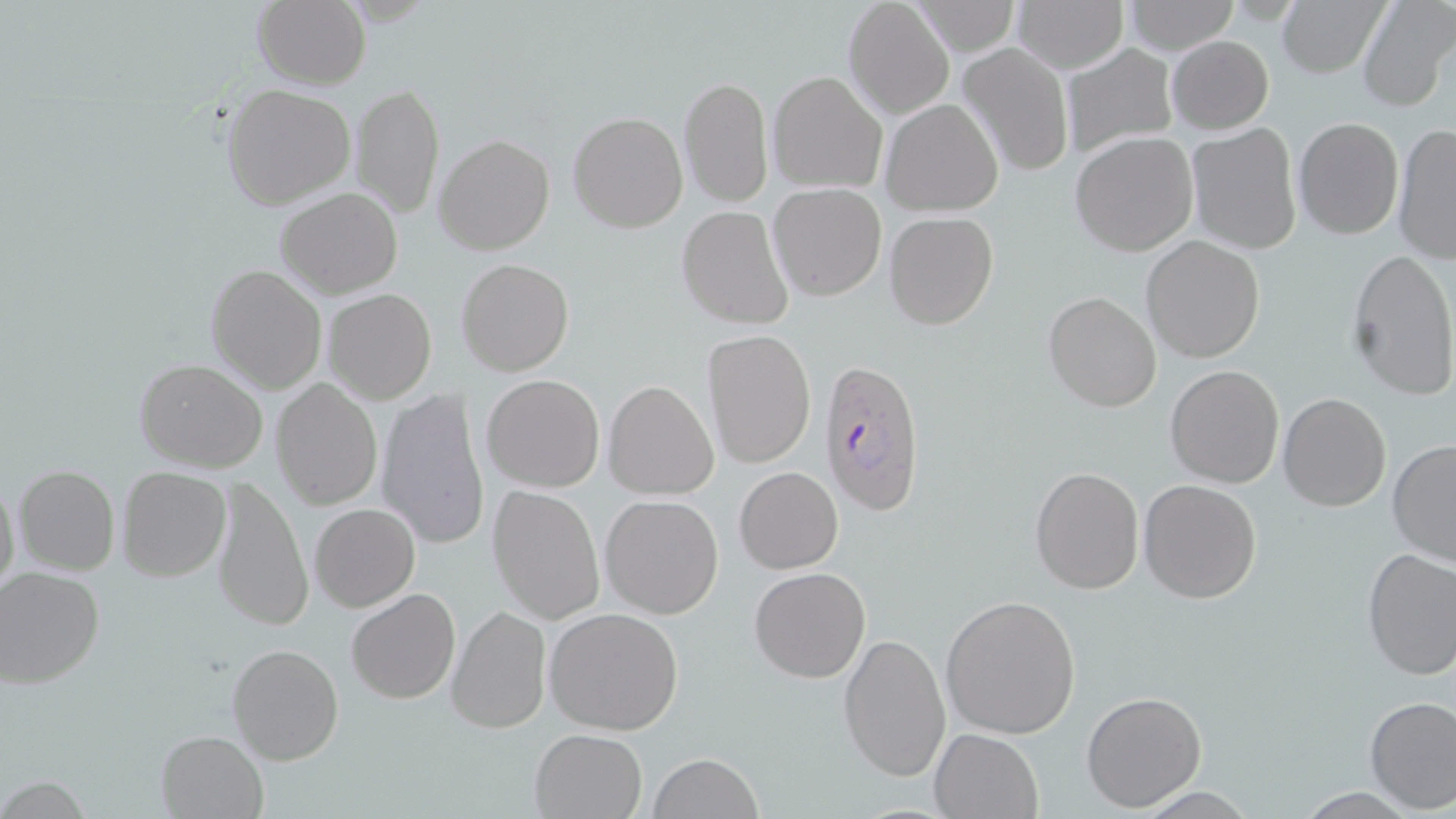

Approximate bounding boxes as (x1,y1)-(x2,y2) corner pairs in pixels. Plasmodium falciparum-infected red blood cell locations: (820,356)-(926,518). Uninfected red blood cell locations: (1010,0)-(1128,73), (1121,0)-(1242,55), (1355,0)-(1453,112), (251,1)-(369,89), (842,1)-(955,120), (911,1)-(1020,57), (1275,1)-(1385,78), (1165,36)-(1274,133), (958,42)-(1075,177), (1062,43)-(1181,157), (766,72)-(888,196), (679,75)-(773,209), (220,83)-(357,211), (352,83)-(444,220), (881,98)-(1005,217), (568,111)-(688,232), (1294,116)-(1405,241), (1186,122)-(1304,254), (1391,124)-(1456,265), (1069,132)-(1199,257), (435,134)-(554,255), (768,183)-(888,300), (274,186)-(403,298), (676,206)-(793,329), (884,211)-(998,330), (1141,235)-(1265,364), (1345,247)-(1456,401), (456,257)-(574,377), (205,263)-(327,394), (321,289)-(438,406), (1043,291)-(1161,411), (702,328)-(816,468), (608,356)-(813,492), (133,358)-(269,473), (1164,364)-(1284,489), (481,373)-(605,492), (271,376)-(384,514), (603,379)-(719,499), (375,388)-(491,551), (1277,392)-(1392,511), (1387,437)-(1456,569), (14,465)-(120,577), (1029,465)-(1145,595), (115,466)-(231,582), (734,466)-(842,573), (0,472)-(20,605), (211,472)-(312,632), (1138,479)-(1263,604), (488,485)-(605,625), (599,494)-(725,620), (310,503)-(420,613), (1359,548)-(1456,679), (749,566)-(872,682), (0,567)-(104,687), (345,587)-(461,705), (939,596)-(1082,741), (446,604)-(552,735), (544,606)-(685,737), (839,632)-(952,781), (226,643)-(344,766), (1081,690)-(1207,811), (1363,695)-(1456,813), (530,728)-(648,818), (930,728)-(1044,818), (155,730)-(269,818), (648,751)-(762,819). Slide-level diagnosis: Plasmodium falciparum. Light microscopy. Captured at 1000x magnification. May-Grünwald-Giemsa stain. Image is 1456×819 pixels. One field of a larger specimen. Thin blood film.